Classify this cell by malaria status.
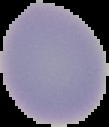
Uninfected.

Summary:
  - Preparation: thin blood smear
  - Image type: cell region segmented out of the field of view; surrounding area masked to black
  - Image size: 109×127 pixels